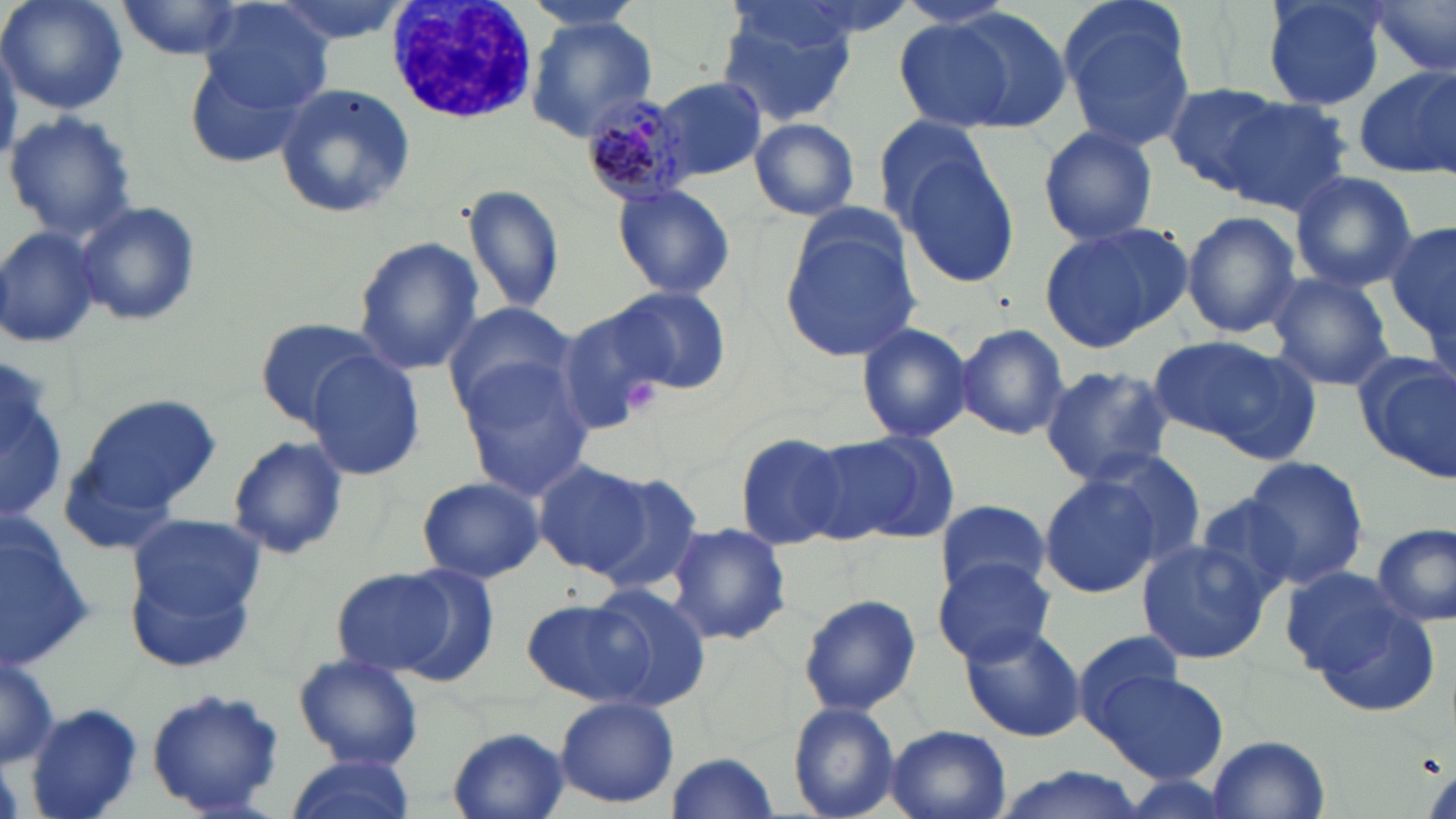
Approximate bounding boxes as named x1/y1/x2/y2 corners in pixels. Platelet locations: (x1=624, y1=379, x2=663, y2=417). Uninfected red blood cell locations: (x1=2, y1=0, x2=127, y2=114), (x1=265, y1=0, x2=412, y2=46), (x1=1055, y1=0, x2=1198, y2=154), (x1=1260, y1=0, x2=1388, y2=111), (x1=1362, y1=0, x2=1456, y2=78), (x1=113, y1=1, x2=244, y2=61), (x1=200, y1=3, x2=335, y2=114), (x1=901, y1=5, x2=1075, y2=137), (x1=717, y1=7, x2=861, y2=123), (x1=524, y1=16, x2=657, y2=143), (x1=0, y1=39, x2=20, y2=168), (x1=185, y1=52, x2=313, y2=169), (x1=1352, y1=64, x2=1456, y2=179), (x1=654, y1=78, x2=766, y2=179), (x1=1163, y1=81, x2=1291, y2=193), (x1=272, y1=84, x2=416, y2=218), (x1=1213, y1=97, x2=1351, y2=214), (x1=4, y1=111, x2=139, y2=241), (x1=870, y1=113, x2=999, y2=232), (x1=749, y1=117, x2=860, y2=220), (x1=1037, y1=125, x2=1160, y2=245), (x1=893, y1=147, x2=1021, y2=289), (x1=1289, y1=171, x2=1419, y2=292), (x1=611, y1=182, x2=736, y2=302), (x1=463, y1=185, x2=567, y2=316), (x1=73, y1=200, x2=202, y2=326), (x1=1182, y1=211, x2=1301, y2=338), (x1=779, y1=221, x2=919, y2=363), (x1=1038, y1=221, x2=1189, y2=353), (x1=1385, y1=221, x2=1456, y2=347), (x1=0, y1=224, x2=106, y2=350), (x1=352, y1=236, x2=484, y2=374), (x1=1265, y1=272, x2=1393, y2=391), (x1=608, y1=288, x2=730, y2=394), (x1=441, y1=299, x2=578, y2=413), (x1=552, y1=307, x2=670, y2=434), (x1=255, y1=316, x2=388, y2=426), (x1=854, y1=321, x2=977, y2=444), (x1=954, y1=323, x2=1071, y2=440), (x1=1148, y1=334, x2=1317, y2=459), (x1=304, y1=350, x2=427, y2=479), (x1=1356, y1=351, x2=1456, y2=479), (x1=0, y1=354, x2=69, y2=523), (x1=456, y1=361, x2=594, y2=498), (x1=1039, y1=365, x2=1175, y2=487), (x1=71, y1=391, x2=220, y2=524), (x1=815, y1=428, x2=958, y2=543), (x1=733, y1=433, x2=850, y2=549), (x1=226, y1=434, x2=348, y2=560), (x1=1087, y1=447, x2=1207, y2=564), (x1=1238, y1=457, x2=1369, y2=590), (x1=535, y1=462, x2=651, y2=575), (x1=582, y1=469, x2=706, y2=595), (x1=1038, y1=474, x2=1166, y2=599), (x1=415, y1=476, x2=545, y2=584), (x1=1189, y1=494, x2=1305, y2=608), (x1=934, y1=498, x2=1050, y2=601), (x1=124, y1=512, x2=265, y2=644), (x1=665, y1=522, x2=793, y2=647), (x1=1374, y1=523, x2=1455, y2=627), (x1=0, y1=525, x2=96, y2=672), (x1=1134, y1=540, x2=1274, y2=665), (x1=932, y1=557, x2=1055, y2=665), (x1=388, y1=562, x2=502, y2=687), (x1=1279, y1=565, x2=1407, y2=674), (x1=331, y1=568, x2=456, y2=677), (x1=586, y1=583, x2=712, y2=707), (x1=798, y1=593, x2=921, y2=717), (x1=522, y1=597, x2=666, y2=708), (x1=1309, y1=603, x2=1442, y2=714), (x1=960, y1=623, x2=1086, y2=742), (x1=1071, y1=629, x2=1188, y2=739), (x1=293, y1=653, x2=425, y2=769), (x1=0, y1=655, x2=59, y2=767), (x1=1098, y1=670, x2=1226, y2=783), (x1=146, y1=686, x2=285, y2=817), (x1=553, y1=696, x2=680, y2=809), (x1=787, y1=701, x2=901, y2=819), (x1=25, y1=703, x2=145, y2=819), (x1=441, y1=726, x2=571, y2=818), (x1=885, y1=727, x2=1011, y2=819), (x1=1209, y1=734, x2=1332, y2=818), (x1=663, y1=751, x2=779, y2=817), (x1=286, y1=755, x2=413, y2=819), (x1=987, y1=767, x2=1153, y2=819). White blood cell locations: (x1=386, y1=0, x2=539, y2=123). Plasmodium malariae-infected red blood cell locations: (x1=583, y1=91, x2=697, y2=203). Slide-level diagnosis: Plasmodium malariae. May-Grünwald-Giemsa stain. Captured at 1000x magnification. Single field of view. Thin blood smear. Light microscopy. Image is 1456×819 pixels.